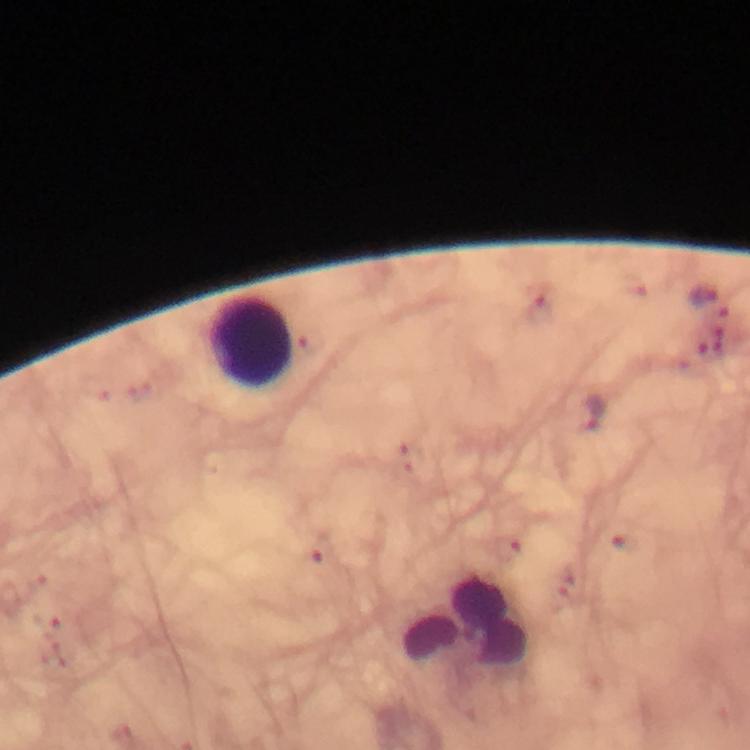

{
  "capture": "smartphone photograph through a microscope",
  "cropped_from": "one field of view",
  "image_size": "750×750 pixels",
  "preparation": "thick blood film",
  "malaria_parasite_locations": "approximate centers as [x, y] in pixels: [540, 311], [593, 412]",
  "stain": "Giemsa",
  "leukocyte_locations": "approximate centers as [x, y] in pixels: [254, 342], [467, 623]",
  "immersion_oil": "used",
  "context": "from a malaria diagnostic workup",
  "magnification": "100x"
}